Locate and identify every blood parasite.
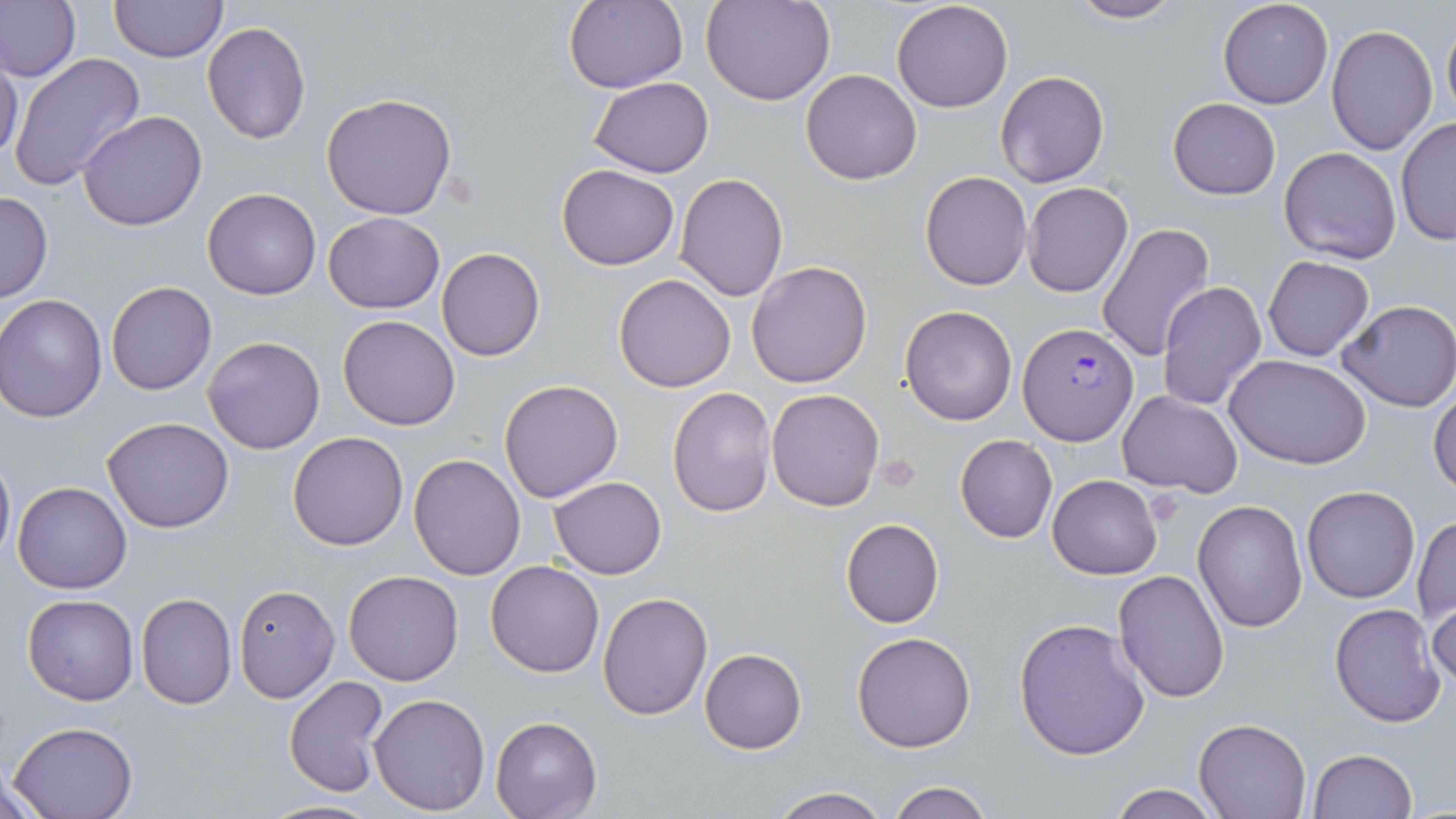
Approximate bounding boxes as (x1,y1)-(x2,y2) corner pairs in pixels.
Plasmodium falciparum-infected red blood cells: (1019,323)-(1137,443).
No Plasmodium ovale, Plasmodium malariae, Plasmodium vivax, Babesia divergens, or Trypanosoma brucei observed.

Summary:
  - Platelet locations: (876,453)-(921,495)
  - Uninfected red blood cell locations: (1,0)-(81,84), (110,0)-(227,64), (565,0)-(689,95), (704,0)-(835,106), (892,0)-(1014,114), (1065,0)-(1183,24), (1217,0)-(1333,110), (1440,7)-(1456,126), (201,20)-(312,145), (1325,23)-(1438,156), (0,50)-(24,166), (8,52)-(145,192), (801,69)-(923,184), (994,70)-(1110,189), (589,77)-(713,177), (319,93)-(458,219), (1167,98)-(1281,200), (77,110)-(207,231), (1395,119)-(1455,246), (1279,145)-(1403,264), (556,164)-(680,270), (920,171)-(1033,292), (676,172)-(789,302), (1022,183)-(1133,297), (202,187)-(321,300), (0,190)-(53,304), (322,212)-(445,314), (1098,223)-(1215,361), (437,247)-(545,361), (1262,254)-(1375,362), (746,261)-(873,387), (613,273)-(738,392), (1157,280)-(1266,409), (106,281)-(216,395), (1,295)-(110,423), (1337,299)-(1456,413), (901,305)-(1017,426), (338,314)-(461,431), (203,335)-(326,455), (1225,353)-(1374,471), (498,380)-(623,502), (1430,384)-(1456,497), (667,387)-(776,517), (767,388)-(885,512), (1117,391)-(1242,495), (102,417)-(234,533), (287,431)-(411,550), (954,434)-(1057,542), (0,445)-(15,568), (409,453)-(526,580), (1047,474)-(1162,578), (550,476)-(667,579), (12,481)-(132,595), (1302,485)-(1420,604), (1193,499)-(1308,633), (1412,516)-(1455,625), (841,518)-(945,629), (484,560)-(605,677), (1112,569)-(1229,702), (343,570)-(464,686), (232,582)-(339,703), (598,590)-(712,721), (135,592)-(237,709), (1427,593)-(1456,693), (23,594)-(138,705), (1329,603)-(1449,728), (1013,617)-(1153,761), (852,631)-(976,753), (700,647)-(807,753), (283,675)-(390,796), (369,692)-(491,813), (491,716)-(601,818), (1193,718)-(1310,819), (9,721)-(139,819), (1306,749)-(1416,819), (5,769)-(55,819), (885,780)-(996,819), (1107,783)-(1221,818), (769,786)-(890,819), (260,798)-(380,818)
  - Slide-level diagnosis: Plasmodium falciparum
  - Modality: light microscopy
  - Image size: 1456×819 pixels
  - Magnification: 1000x
  - Stain: May-Grünwald-Giemsa
  - Field of view: one of a larger specimen
  - Preparation: thin blood smear